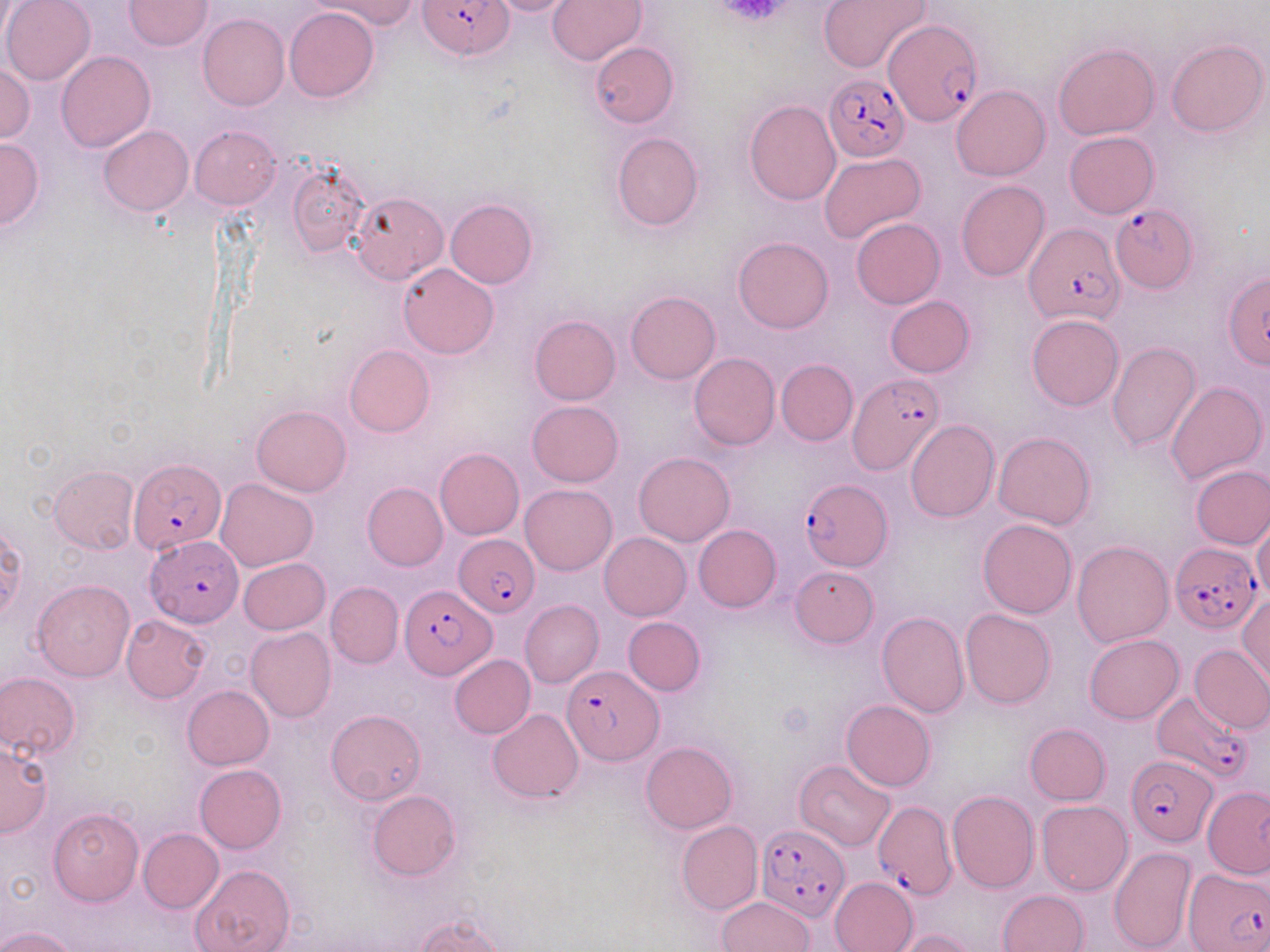

Approximate bounding boxes as (x1,y1)-(x2,y2) corner pairs in pixels. Plasmodium falciparum-infected red blood cell locations: (419,1)-(512,60), (891,19)-(985,125), (824,74)-(910,161), (1108,203)-(1198,292), (1025,222)-(1122,326), (849,373)-(945,476), (130,457)-(225,556), (799,479)-(892,571), (454,534)-(540,616), (144,535)-(245,626), (1169,543)-(1260,633), (399,584)-(498,678), (562,665)-(662,764), (1153,691)-(1248,781), (1126,755)-(1217,845), (872,800)-(956,901), (757,824)-(851,921), (1184,867)-(1270,950). Platelet locations: (715,1)-(795,26). Uninfected red blood cell locations: (1,0)-(96,85), (125,0)-(212,50), (313,0)-(417,34), (484,0)-(579,18), (547,0)-(647,65), (818,0)-(932,74), (285,7)-(378,102), (198,13)-(288,111), (1167,39)-(1268,137), (590,42)-(678,128), (1053,43)-(1159,139), (56,50)-(156,151), (0,63)-(35,143), (951,85)-(1051,181), (744,100)-(840,206), (99,125)-(193,216), (190,125)-(280,210), (611,132)-(704,231), (1064,132)-(1158,218), (0,138)-(43,229), (819,153)-(926,244), (287,158)-(368,259), (955,180)-(1051,281), (351,192)-(448,284), (446,199)-(538,289), (852,217)-(945,308), (733,236)-(832,334), (398,262)-(499,359), (626,291)-(720,383), (884,296)-(976,377), (1026,314)-(1125,411), (530,315)-(620,406), (1106,341)-(1200,450), (344,344)-(434,436), (688,353)-(779,449), (775,359)-(857,446), (1167,382)-(1266,484), (528,400)-(623,485), (251,405)-(351,496), (906,421)-(1000,522), (993,432)-(1095,529), (435,448)-(524,540), (634,453)-(735,546), (1191,465)-(1270,548), (48,466)-(139,553), (215,478)-(319,571), (362,482)-(447,571), (520,484)-(616,575), (1252,516)-(1270,600), (977,518)-(1077,618), (692,524)-(781,611), (599,532)-(691,620), (1072,540)-(1173,646), (238,558)-(330,635), (791,565)-(878,647), (32,580)-(135,682), (326,581)-(403,669), (1239,594)-(1270,687), (520,599)-(604,686), (960,608)-(1056,708), (876,610)-(970,717), (121,615)-(210,702), (623,617)-(704,695), (246,626)-(336,722), (1084,634)-(1184,723), (1189,644)-(1270,733), (450,655)-(536,739), (0,672)-(80,758), (182,685)-(273,769), (841,700)-(935,790), (325,709)-(425,805), (487,709)-(583,802), (1024,723)-(1110,806), (0,742)-(51,837), (641,742)-(737,834), (795,760)-(895,851), (195,763)-(286,853), (1203,784)-(1270,878), (367,790)-(460,881), (947,791)-(1038,893), (1036,801)-(1132,895), (47,806)-(144,906), (677,821)-(762,915), (137,828)-(223,913), (1109,846)-(1196,951), (190,863)-(295,952), (830,876)-(918,952), (997,889)-(1089,952), (716,897)-(815,951), (415,916)-(506,952), (0,926)-(78,952), (894,929)-(978,951). Slide-level diagnosis: Plasmodium falciparum. Thin blood film. Image is 1270×952 pixels. Optical microscopy. May-Grünwald-Giemsa stain. One field of a larger specimen. 1000x magnification.